Look for Plasmodium parasites.
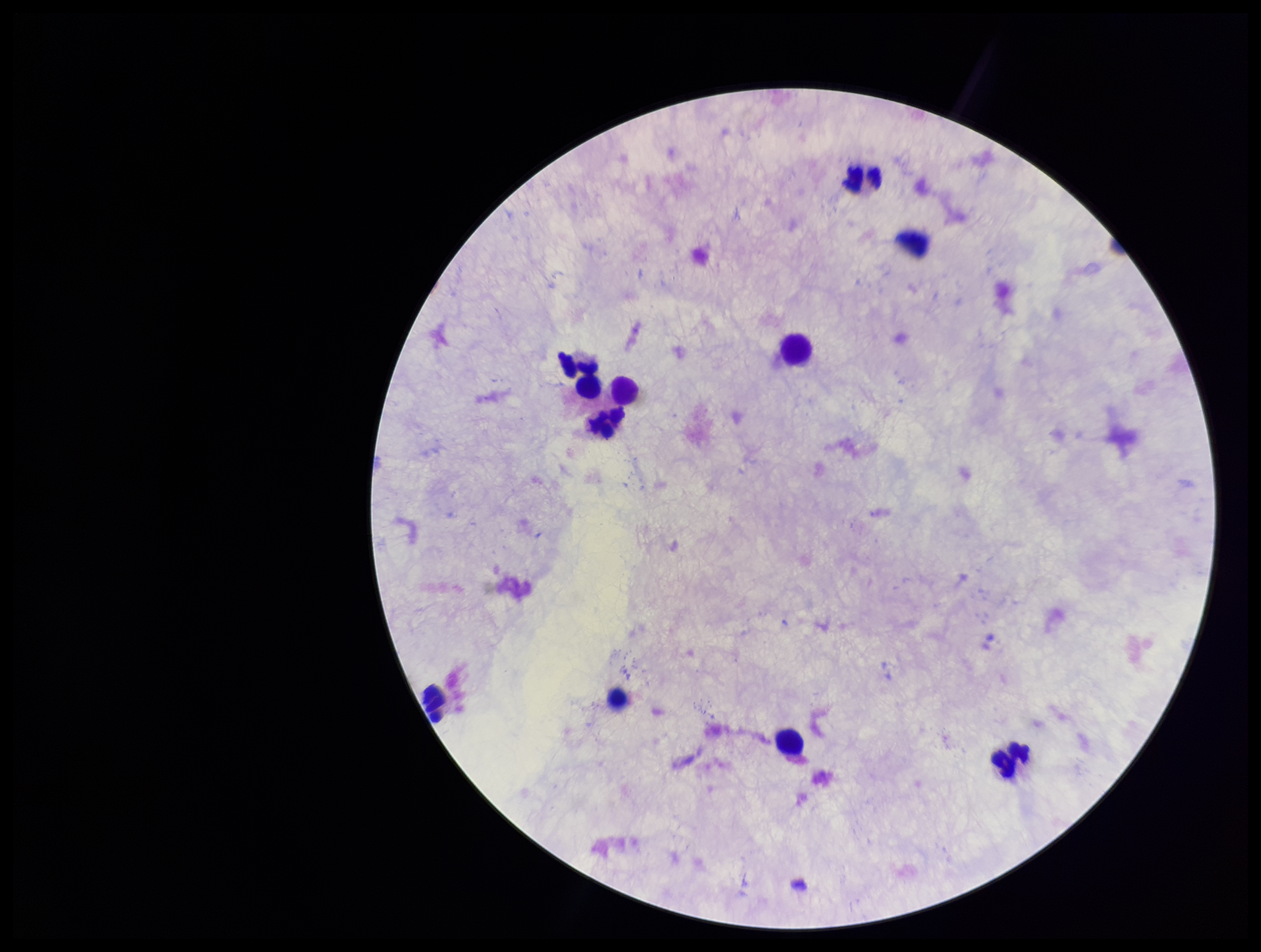

None identified.

Summary:
  - Preparation: thick blood smear
  - Field of view: single
  - Image size: 1261×952 pixels
  - Patient malaria status: negative
  - Parasite count: 0
  - Leukocyte count: 10
  - Capture: smartphone photograph through the microscope eyepiece
  - Stain: Giemsa